Classify this cell by malaria status.
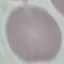

Uninfected.

preparation: thin blood film
stain: Giemsa
image_type: cell patch, automatically extracted from a larger field of view and resized to 64 × 64 pixels
capture: smartphone through the microscope eyepiece